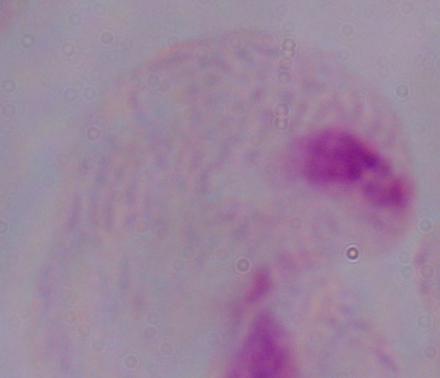

{
  "magnification": "1000x",
  "modality": "micrograph",
  "identification": "trichomonad"
}